Identify the parasite.
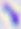
Toxoplasma gondii.

modality = photomicrograph
magnification = 400x